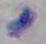
Summary:
  - Identification: Toxoplasma gondii
  - Magnification: 1000x
  - Modality: micrograph